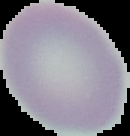

preparation = thin blood smear
image size = 130×136 pixels
image type = cell region segmented out of the field of view; surrounding area masked to black
malaria status = uninfected